State which cell type is depicted.
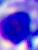
A leukocyte.

Summary:
  - Modality: micrograph
  - Magnification: 400x